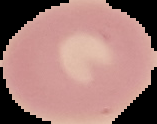

preparation = thin blood smear
image size = 157×124 pixels
result = no malaria parasites seen
image type = cell region segmented out of the field of view; surrounding area masked to black